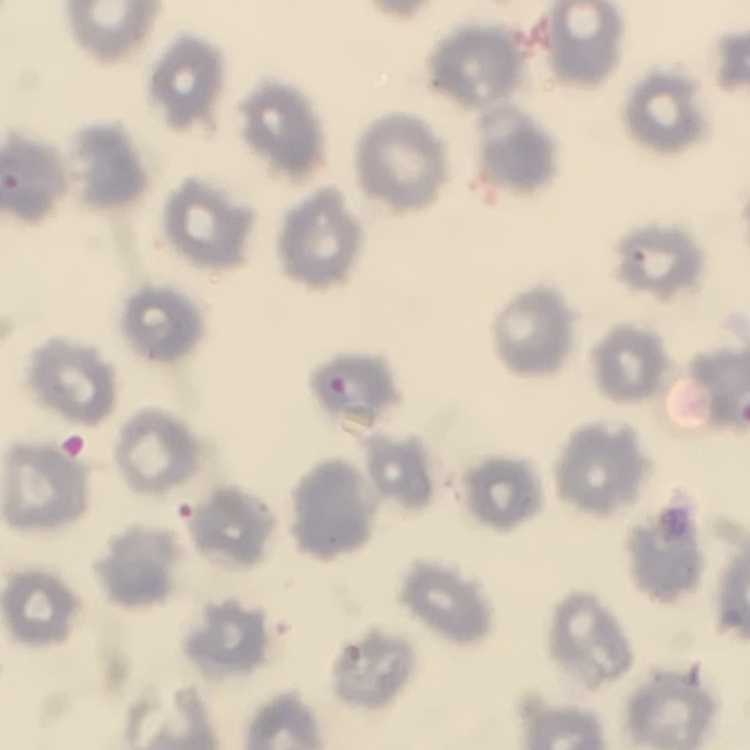
red_blood_cell_morphology: no rouleaux formation
stain: Field's or Giemsa
image_type: one tile cut from a larger photomicrograph
preparation: thin peripheral smear